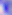

modality: photomicrograph
identification: Toxoplasma gondii
magnification: 400x